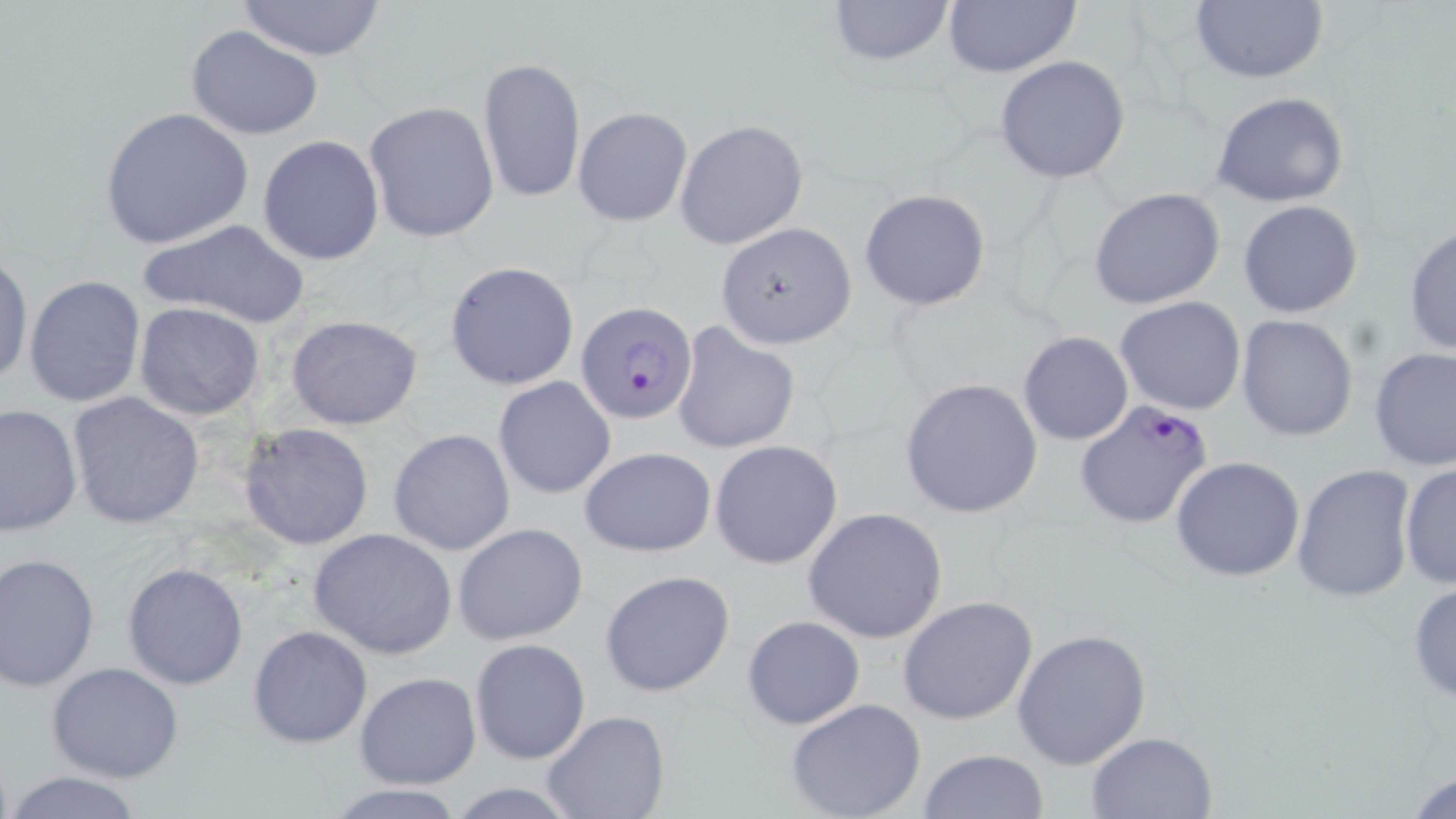
Approximate bounding boxes as (x1, y1, x2, y2) in pixels. Plasmodium falciparum-infected red blood cell locations: (575, 302, 702, 424), (1075, 400, 1214, 530). Uninfected red blood cell locations: (232, 0, 388, 61), (823, 0, 959, 67), (941, 0, 1083, 79), (1188, 1, 1330, 85), (185, 24, 323, 139), (994, 55, 1131, 184), (477, 56, 586, 204), (1211, 93, 1351, 208), (364, 101, 500, 242), (571, 105, 692, 227), (99, 107, 254, 251), (674, 119, 807, 251), (257, 135, 386, 266), (1088, 188, 1227, 310), (859, 189, 991, 311), (1237, 199, 1364, 318), (139, 218, 312, 330), (715, 222, 857, 349), (1405, 223, 1456, 361), (0, 251, 32, 389), (444, 260, 581, 392), (24, 274, 146, 409), (1115, 295, 1247, 416), (135, 302, 266, 421), (285, 314, 424, 430), (1237, 314, 1358, 442), (669, 321, 801, 456), (1017, 330, 1134, 447), (1369, 346, 1456, 473), (494, 376, 615, 500), (899, 378, 1044, 520), (67, 392, 204, 528), (1, 403, 82, 537), (240, 422, 374, 550), (389, 427, 514, 557), (710, 441, 842, 569), (579, 447, 717, 557), (1170, 456, 1306, 580), (1290, 464, 1416, 601), (1399, 465, 1456, 590), (802, 507, 949, 644), (452, 522, 588, 645), (308, 527, 457, 660), (0, 552, 100, 692), (122, 562, 249, 691), (598, 569, 735, 698), (1407, 579, 1456, 704), (897, 596, 1039, 725), (741, 615, 865, 730), (248, 626, 373, 748), (1011, 626, 1153, 769), (469, 638, 591, 765), (45, 662, 186, 784), (355, 673, 480, 789), (785, 699, 927, 819), (541, 711, 670, 819), (1085, 730, 1217, 817), (917, 749, 1050, 819), (1404, 764, 1456, 819), (0, 772, 152, 818), (321, 782, 469, 817). Slide-level diagnosis: Plasmodium falciparum. 1000x magnification. Thin blood film. Optical microscopy. Image is 1456×819 pixels. May-Grünwald-Giemsa-stained preparation. Single field of view.